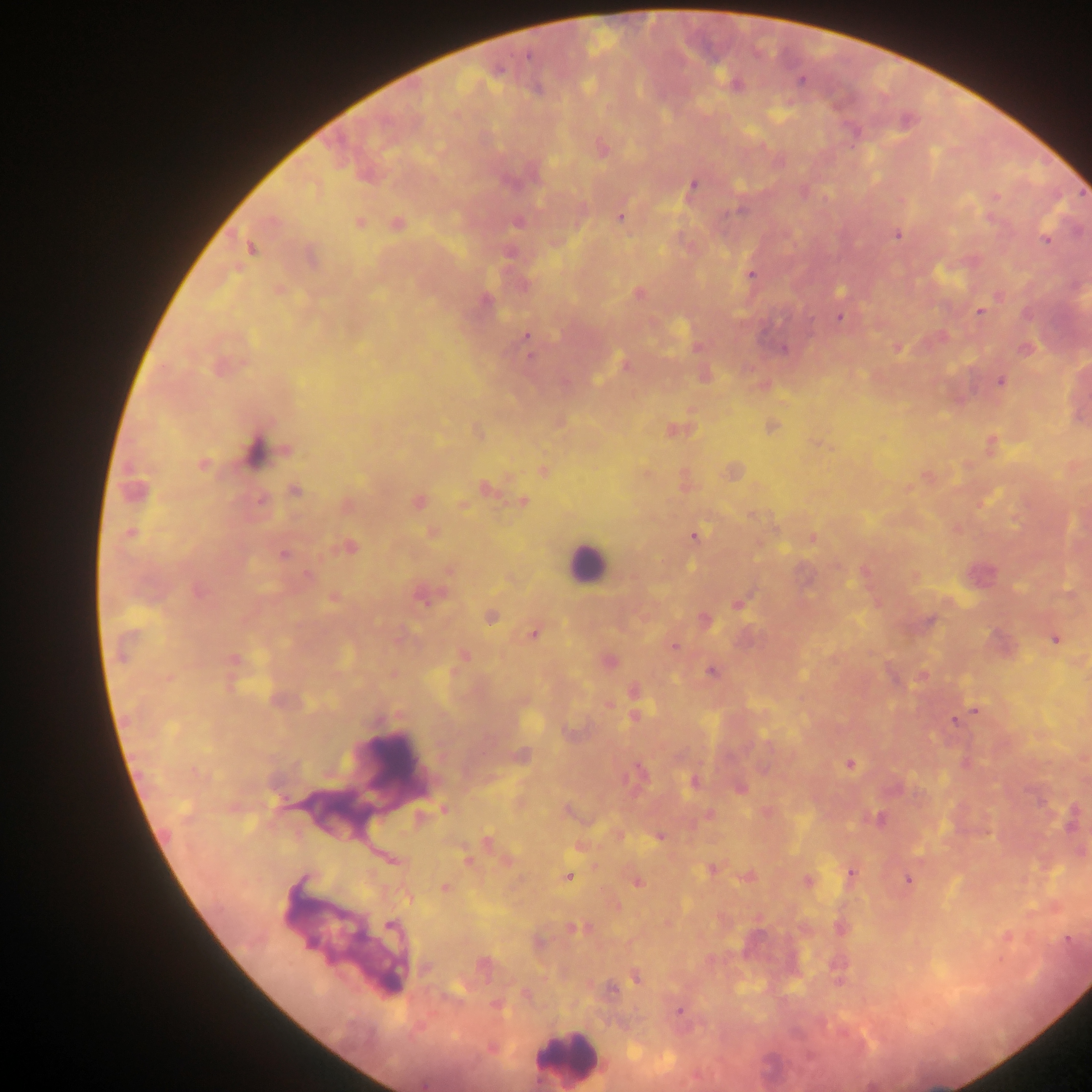 Approximate centers as {x, y} in pixels. Leukocyte locations: {587, 563}, {389, 762}, {333, 813}, {349, 934}, {567, 1057}. Plasmodium parasite locations: {800, 80}, {736, 84}, {600, 148}, {692, 186}, {995, 197}, {901, 200}, {620, 217}, {518, 221}, {358, 222}, {396, 224}, {897, 234}, {1046, 240}, {250, 248}, {310, 256}, {751, 275}, {277, 289}, {840, 290}, {638, 292}, {1000, 295}, {484, 299}, {978, 311}, {839, 316}, {526, 336}, {942, 337}, {697, 346}, {897, 347}, {784, 349}, {1025, 349}, {530, 356}, {625, 364}, {219, 367}, {705, 375}, {1000, 381}, {565, 382}, {763, 385}, {559, 422}, {771, 426}, {674, 430}, {477, 432}, {818, 443}, {992, 444}, {255, 450}, {202, 464}, {543, 471}, {733, 471}, {645, 473}, {927, 476}, {684, 482}, {485, 488}, {135, 490}, {294, 490}, {261, 501}, {417, 501}, {523, 501}, {983, 501}, {462, 504}, {346, 505}, {956, 528}, {432, 532}, {131, 534}, {694, 536}, {811, 538}, {349, 547}, {283, 554}, {450, 569}, {865, 571}, {307, 575}, {979, 575}, {914, 576}, {198, 591}, {423, 593}, {334, 597}, {738, 603}, {490, 615}, {704, 620}, {929, 621}, {534, 632}, {1056, 638}, {1001, 645}, {673, 646}, {463, 655}, {608, 660}, {234, 661}, {712, 670}, {392, 673}, {922, 676}, {168, 678}, {633, 690}, {523, 700}, {608, 704}, {975, 710}, {634, 715}, {954, 720}, {570, 732}, {520, 755}, {965, 762}, {850, 764}, {637, 773}, {694, 781}, {739, 788}, {443, 809}, {567, 810}, {765, 812}, {709, 814}, {878, 818}, {1072, 820}, {617, 834}, {659, 836}, {486, 842}, {580, 846}, {1080, 851}, {467, 860}, {506, 861}, {711, 869}, {851, 873}, {567, 876}, {748, 876}, {908, 879}, {637, 881}, {808, 882}, {444, 888}, {614, 904}, {668, 922}, {391, 925}, {841, 927}, {577, 928}, {1005, 937}, {1067, 938}, {537, 942}, {482, 965}, {636, 976}, {611, 988}, {525, 993}, {496, 1005}, {679, 1011}, {491, 1048}. Thick blood smear. Photographed through a microscope with a mobile-phone camera. One field of view. Sample from Ghana. Image is 1092×1092 pixels.